Locate every Plasmodium vivax-infected red blood cell.
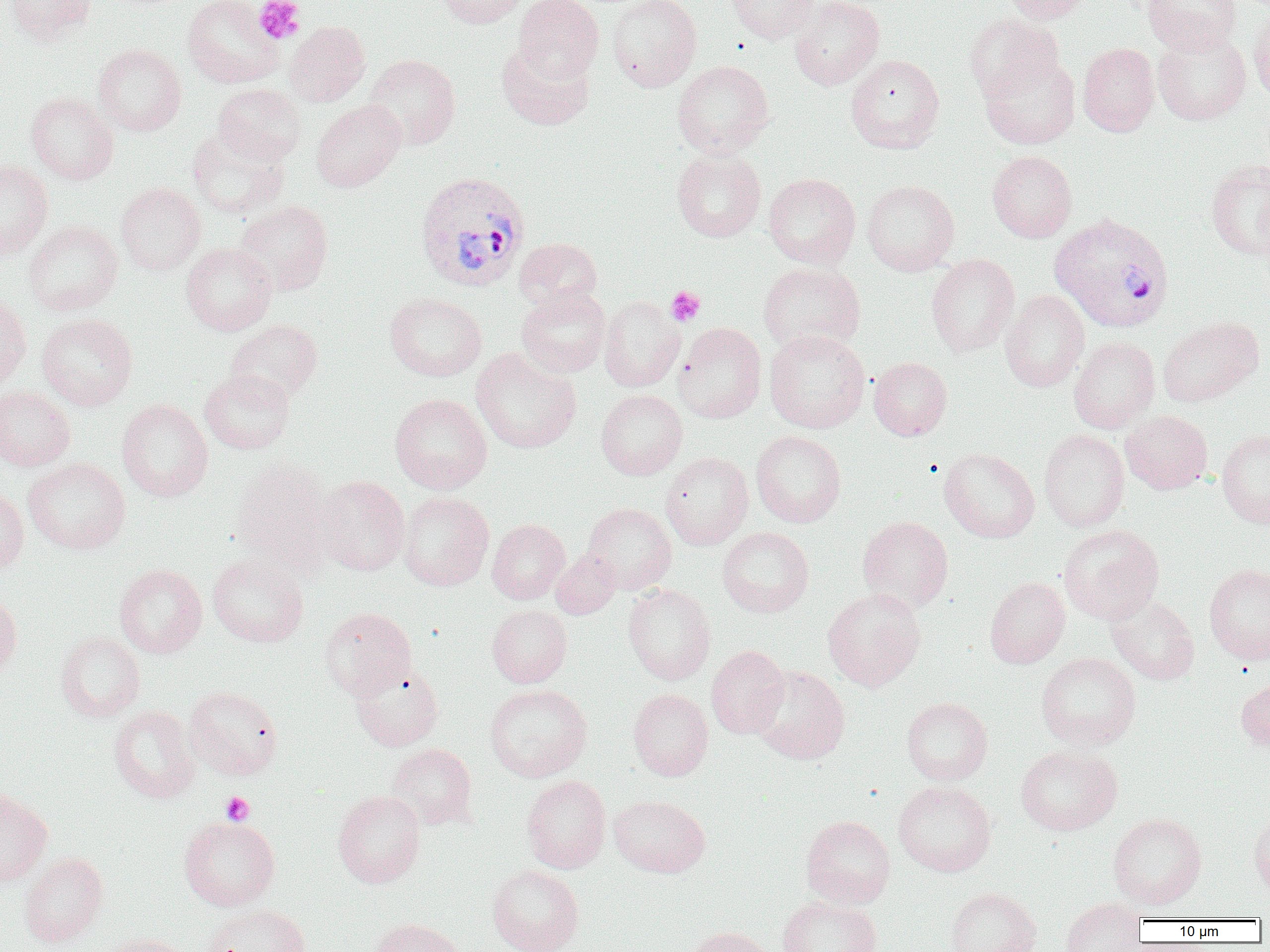

Approximate bounding boxes as [x1, y1, x2, y2] in pixels.
Plasmodium vivax-infected red blood cells: [414, 171, 531, 292], [1050, 213, 1174, 332].

Uninfected red blood cell locations: [5, 0, 96, 45], [182, 0, 284, 88], [436, 0, 528, 28], [512, 0, 603, 83], [606, 0, 701, 92], [726, 0, 819, 44], [789, 0, 884, 90], [999, 0, 1093, 23], [1143, 0, 1240, 54], [1248, 8, 1270, 104], [965, 13, 1063, 101], [284, 21, 370, 106], [1152, 28, 1251, 125], [496, 40, 595, 130], [1078, 42, 1159, 137], [92, 43, 187, 136], [979, 52, 1080, 149], [363, 54, 461, 151], [846, 54, 945, 154], [672, 60, 774, 158], [213, 84, 307, 164], [25, 92, 118, 184], [311, 100, 406, 191], [187, 129, 289, 219], [671, 148, 766, 242], [987, 151, 1077, 242], [1206, 160, 1270, 260], [0, 162, 53, 260], [763, 173, 861, 268], [861, 180, 960, 276], [115, 181, 206, 275], [235, 200, 333, 295], [24, 220, 123, 316], [514, 237, 602, 311], [181, 242, 277, 335], [926, 254, 1019, 357], [758, 262, 866, 353], [516, 285, 611, 377], [1001, 290, 1089, 392], [0, 293, 31, 388], [385, 293, 487, 381], [599, 296, 685, 392], [37, 313, 138, 411], [1158, 316, 1263, 407], [226, 320, 323, 402], [674, 322, 767, 423], [764, 330, 870, 433], [1069, 336, 1160, 433], [470, 347, 582, 454], [868, 357, 952, 440], [199, 369, 295, 455], [0, 386, 75, 470], [596, 389, 687, 480], [390, 393, 492, 494], [117, 399, 213, 502], [1120, 410, 1212, 494], [1039, 430, 1129, 532], [1217, 430, 1270, 528], [751, 431, 846, 527], [940, 447, 1040, 542], [660, 452, 754, 550], [23, 457, 130, 554], [231, 458, 336, 573], [315, 475, 411, 575], [0, 487, 29, 573], [398, 491, 494, 591], [582, 502, 677, 594], [857, 516, 953, 613], [486, 518, 570, 604], [1059, 525, 1164, 624], [717, 527, 814, 617], [551, 550, 620, 620], [207, 554, 308, 647], [1204, 563, 1270, 665], [114, 564, 207, 658], [984, 576, 1070, 668], [623, 584, 716, 685], [822, 587, 926, 691], [0, 591, 22, 681], [1105, 594, 1199, 684], [487, 604, 572, 688], [319, 607, 416, 699], [55, 630, 145, 722], [706, 645, 789, 738], [1036, 651, 1141, 750], [349, 660, 444, 751], [750, 665, 850, 764], [1236, 679, 1270, 752], [484, 684, 593, 782], [185, 686, 283, 779], [628, 688, 713, 781], [901, 697, 993, 785], [108, 705, 200, 803], [386, 743, 477, 830], [1015, 745, 1122, 835], [522, 775, 611, 873], [893, 780, 996, 877], [0, 788, 52, 887], [332, 790, 426, 888], [609, 794, 710, 877], [1248, 809, 1270, 896], [1107, 812, 1206, 909], [178, 815, 280, 911], [801, 815, 895, 908], [19, 851, 108, 946], [486, 864, 584, 952], [945, 887, 1041, 952], [777, 895, 882, 952], [1060, 898, 1146, 951], [202, 904, 311, 952], [368, 917, 465, 952], [682, 926, 776, 952], [98, 932, 193, 952]. Platelet locations: [253, 0, 305, 44], [666, 286, 705, 326], [221, 792, 254, 825]. Slide-level diagnosis: Plasmodium vivax. One field of a larger specimen. Image is 1270×952 pixels. 1000x magnification. Optical microscopy. Thin blood smear.